Name the parasite shown.
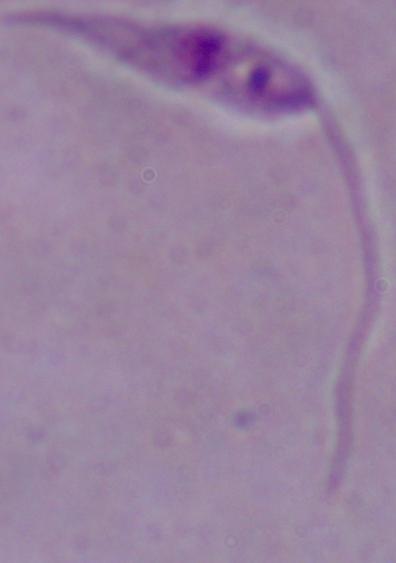
Leishmania.

Summary:
  - Modality: micrograph
  - Magnification: 1000x